Locate every Trypanosoma brucei.
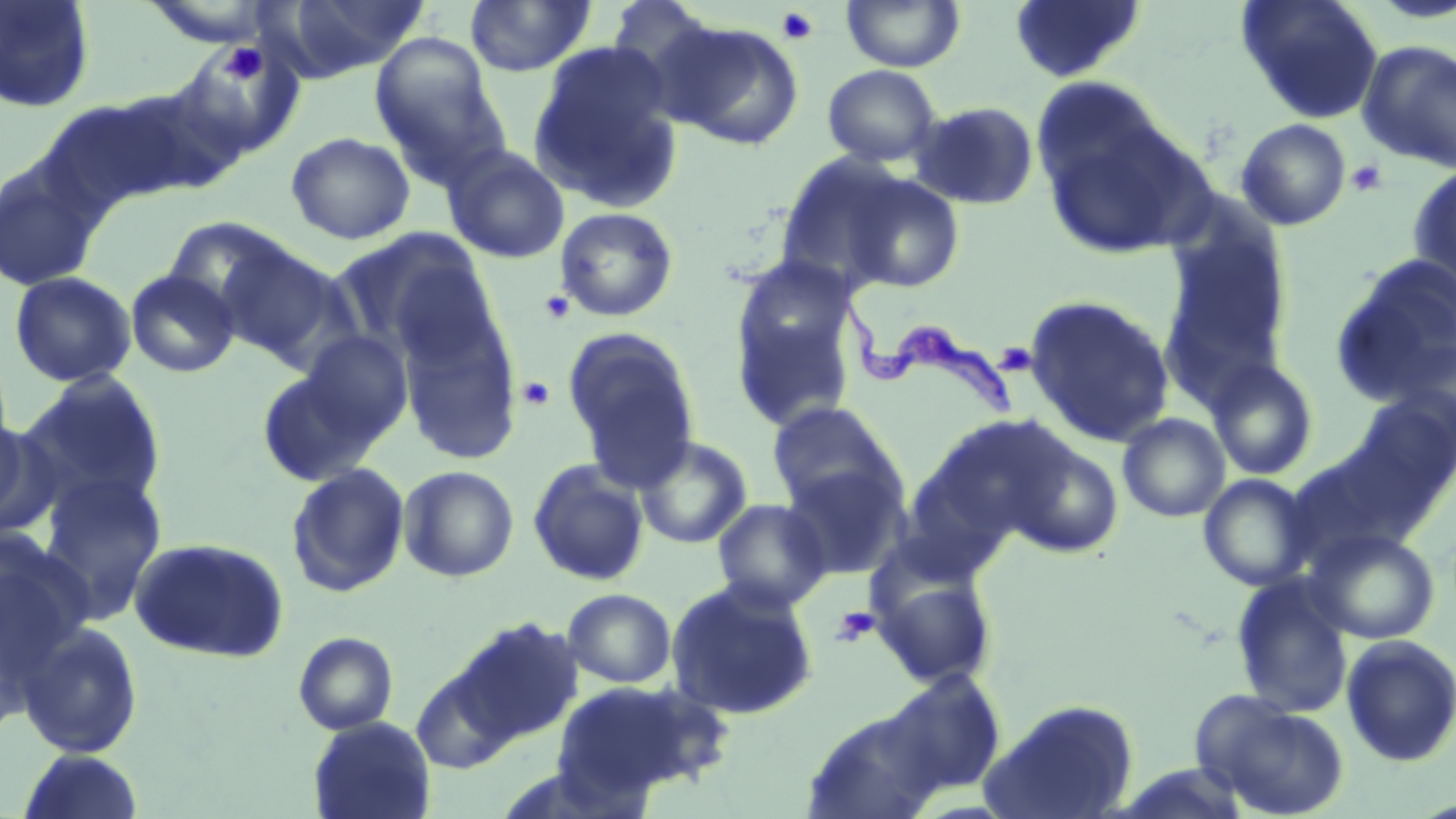

Approximate bounding boxes as [x1, y1, x2, y2] in pixels.
Trypanosoma brucei: [834, 280, 1014, 420].

Summary:
  - Uninfected red blood cell locations: [0, 0, 95, 113], [276, 0, 427, 80], [464, 0, 596, 78], [841, 0, 965, 72], [1008, 0, 1146, 83], [1236, 0, 1384, 124], [146, 2, 275, 48], [657, 19, 806, 151], [370, 35, 508, 185], [529, 40, 686, 210], [1356, 40, 1456, 173], [822, 64, 941, 167], [109, 83, 243, 198], [1036, 94, 1209, 261], [42, 96, 189, 211], [910, 100, 1040, 210], [1235, 118, 1352, 231], [285, 131, 415, 244], [442, 144, 571, 265], [773, 154, 909, 293], [0, 162, 102, 292], [1407, 164, 1456, 297], [841, 172, 966, 294], [555, 207, 679, 322], [1159, 215, 1295, 392], [163, 216, 295, 321], [333, 227, 497, 364], [213, 239, 352, 368], [1329, 255, 1456, 407], [729, 262, 861, 429], [125, 269, 240, 378], [8, 271, 137, 388], [1023, 294, 1176, 447], [396, 300, 522, 466], [562, 327, 701, 485], [298, 331, 413, 444], [1387, 338, 1455, 446], [1205, 357, 1320, 480], [256, 369, 382, 487], [17, 374, 169, 517], [1349, 394, 1456, 505], [766, 401, 903, 513], [1118, 413, 1230, 522], [0, 415, 54, 537], [632, 435, 753, 549], [1004, 436, 1124, 559], [527, 459, 650, 587], [779, 460, 911, 581], [285, 462, 411, 598], [398, 465, 519, 583], [36, 470, 168, 624], [1197, 474, 1317, 592], [712, 498, 832, 612], [1307, 527, 1441, 645], [0, 529, 92, 667], [128, 537, 290, 663], [870, 564, 999, 688], [1230, 574, 1354, 718], [665, 576, 820, 721], [562, 588, 676, 688], [453, 617, 582, 742], [17, 621, 144, 759], [293, 632, 399, 736], [1340, 634, 1456, 767], [411, 668, 513, 775], [878, 669, 1006, 800], [552, 678, 726, 799], [1198, 696, 1351, 818], [982, 698, 1139, 819], [802, 707, 949, 818], [308, 716, 436, 819], [16, 748, 144, 818]
  - Platelet locations: [775, 6, 820, 46], [219, 42, 268, 85], [1346, 159, 1387, 197], [539, 291, 574, 324], [998, 344, 1033, 376], [516, 375, 556, 410], [832, 606, 880, 646]
  - Slide-level diagnosis: Trypanosoma brucei
  - Stain: May-Grünwald-Giemsa
  - Magnification: 1000x
  - Field of view: single
  - Modality: optical microscopy
  - Preparation: thin blood smear
  - Image size: 1456×819 pixels